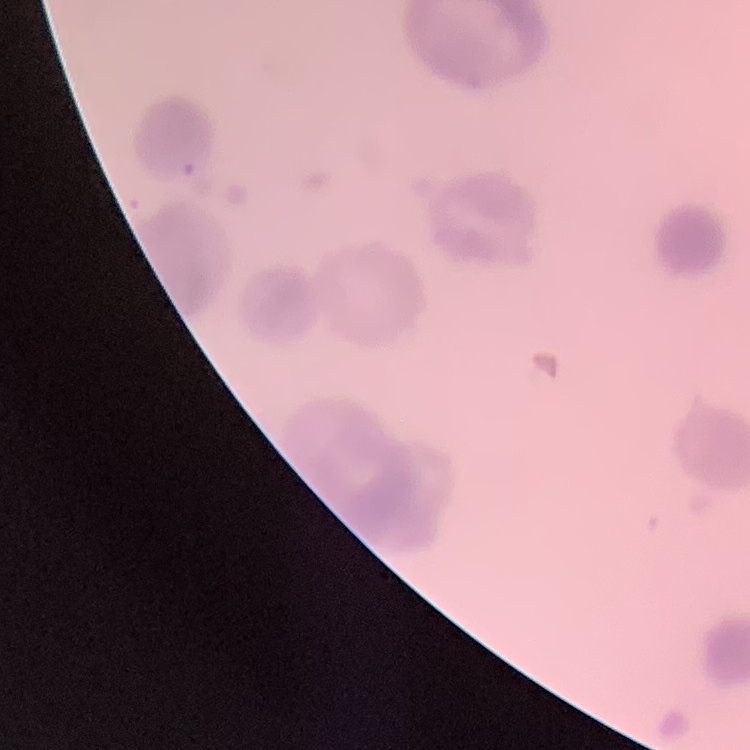 The erythrocytes exhibit rouleaux formation. One tile cut from a larger photomicrograph. Thin blood smear. Field's or Giemsa stain.